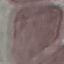

result: no malaria parasites seen
stain: Giemsa
image_type: automatically extracted cell patch, resized to 64 × 64 pixels
capture: smartphone camera at the microscope eyepiece
preparation: thin smear